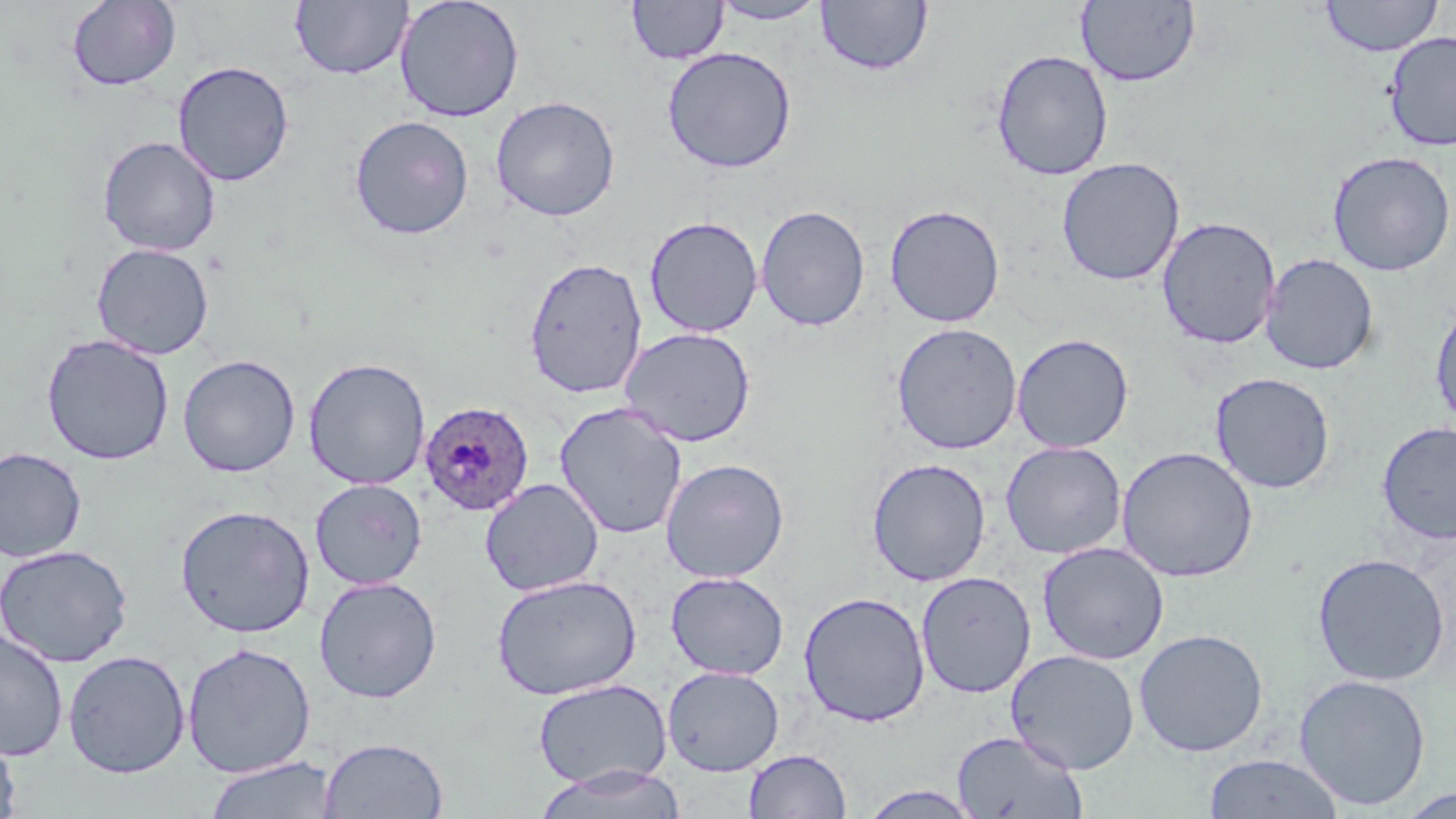
Approximate bounding boxes as [x1, y1, x2, y2] in pixels. Plasmodium ovale-infected red blood cell locations: [418, 401, 534, 517]. Uninfected red blood cell locations: [66, 0, 181, 92], [394, 0, 525, 123], [815, 0, 933, 77], [1319, 0, 1444, 57], [290, 1, 412, 80], [626, 1, 728, 65], [711, 1, 828, 25], [1076, 1, 1201, 87], [1384, 31, 1456, 152], [661, 46, 797, 173], [991, 49, 1113, 181], [172, 60, 295, 186], [490, 95, 621, 221], [349, 115, 475, 240], [98, 136, 221, 256], [1326, 150, 1456, 276], [1056, 157, 1185, 286], [756, 204, 871, 331], [884, 204, 1006, 328], [644, 215, 763, 337], [1156, 216, 1281, 349], [91, 243, 214, 360], [1260, 253, 1379, 375], [524, 256, 648, 398], [1429, 299, 1456, 432], [891, 322, 1022, 455], [619, 326, 756, 447], [40, 333, 175, 466], [1011, 333, 1134, 453], [177, 354, 301, 477], [302, 357, 431, 490], [1210, 372, 1335, 494], [554, 401, 688, 539], [1376, 421, 1456, 546], [1001, 441, 1127, 560], [1116, 445, 1258, 583], [0, 446, 88, 563], [866, 457, 991, 586], [660, 458, 790, 583], [310, 478, 427, 590], [480, 478, 604, 596], [175, 504, 315, 638], [1037, 541, 1169, 665], [0, 543, 133, 667], [1312, 552, 1450, 686], [665, 571, 789, 680], [915, 571, 1036, 698], [491, 574, 642, 701], [313, 576, 442, 703], [798, 591, 930, 727], [0, 627, 69, 763], [1133, 628, 1269, 757], [181, 642, 316, 778], [1005, 649, 1140, 774], [63, 650, 191, 779], [662, 665, 785, 776], [1293, 673, 1431, 811], [532, 678, 672, 790], [0, 731, 22, 819], [950, 732, 1089, 817], [319, 736, 449, 818], [743, 748, 852, 819], [1202, 753, 1346, 818], [203, 755, 339, 819], [532, 763, 688, 819], [855, 785, 984, 818], [1396, 785, 1455, 817]. Slide-level diagnosis: Plasmodium ovale. 1000x magnification. May-Grünwald-Giemsa stain. One field of a larger specimen. Image is 1456×819 pixels. Thin blood smear. Optical microscopy.